Assess this cell for malaria.
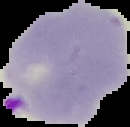

It is parasitized.

preparation = thin blood smear
image type = cell region segmented out of the field of view; surrounding area masked to black
image size = 130×127 pixels